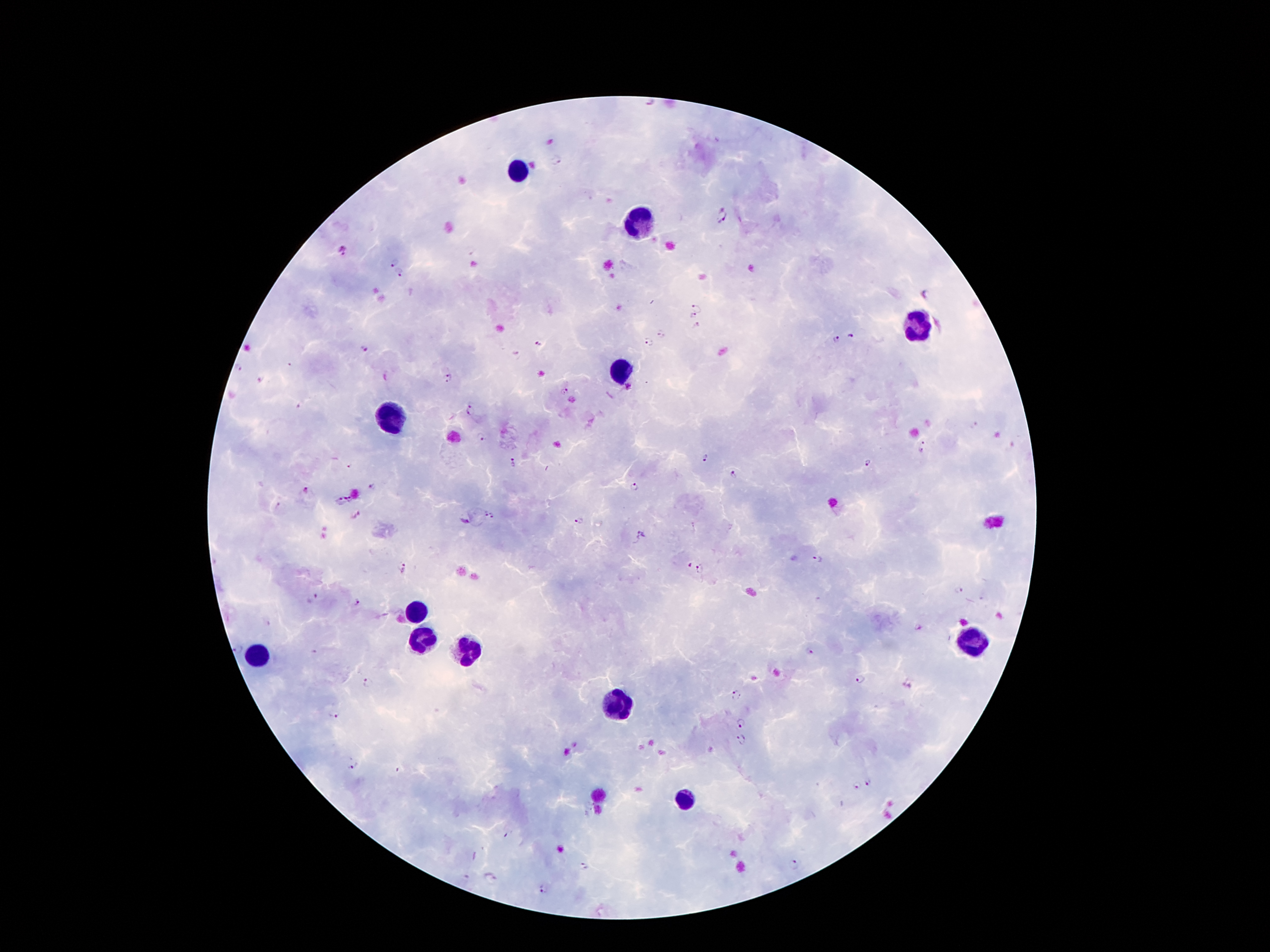
Approximate centers as {x, y} in pixels. Leukocyte locations: {518, 172}, {637, 222}, {920, 326}, {620, 373}, {390, 419}, {416, 610}, {423, 641}, {975, 643}, {465, 652}, {259, 654}, {620, 708}, {686, 800}. Plasmodium parasite locations: {556, 163}, {723, 217}, {342, 251}, {394, 262}, {400, 273}, {698, 307}, {692, 315}, {697, 325}, {662, 335}, {852, 335}, {834, 338}, {649, 343}, {539, 344}, {364, 348}, {238, 367}, {449, 379}, {260, 380}, {564, 393}, {470, 411}, {480, 438}, {923, 446}, {703, 459}, {513, 463}, {868, 463}, {351, 466}, {733, 475}, {372, 487}, {634, 487}, {306, 490}, {349, 500}, {341, 503}, {279, 506}, {484, 514}, {493, 516}, {580, 520}, {464, 522}, {641, 535}, {817, 560}, {689, 567}, {405, 568}, {701, 568}, {959, 592}, {312, 598}, {357, 603}, {238, 649}, {811, 651}, {861, 679}, {367, 682}, {737, 696}, {335, 716}, {740, 722}, {742, 739}, {351, 766}, {870, 782}, {856, 787}, {794, 862}, {584, 866}, {543, 889}. 100x magnification. Thick blood film. Patient malaria status: positive for Plasmodium falciparum. Single field of view. Giemsa-stained preparation. Smartphone photograph taken through the microscope eyepiece. Image is 1270×952 pixels.